Assess the morphology of the erythrocytes.
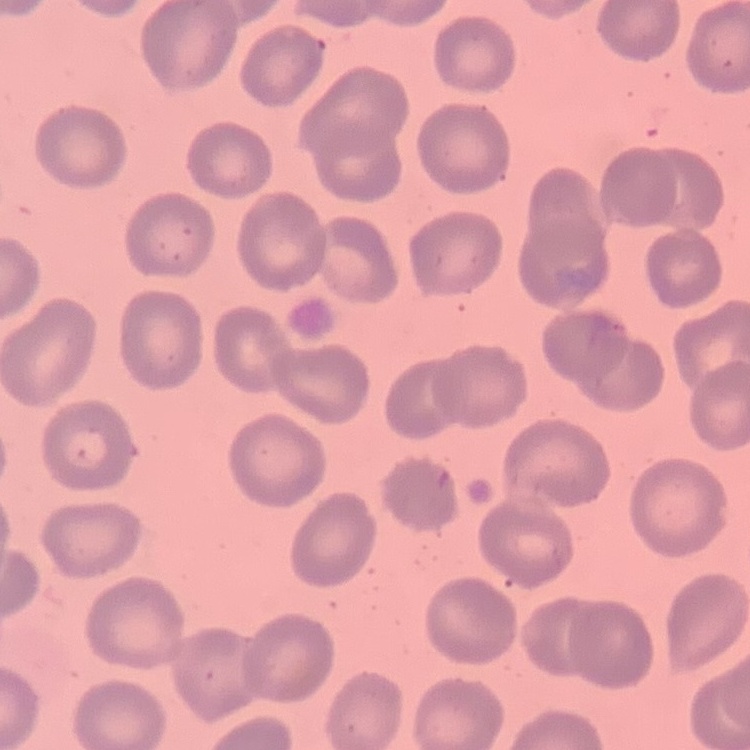
No rouleaux formation.

preparation = thin blood smear
image type = square crop of a larger photomicrograph
stain = Field's or Giemsa